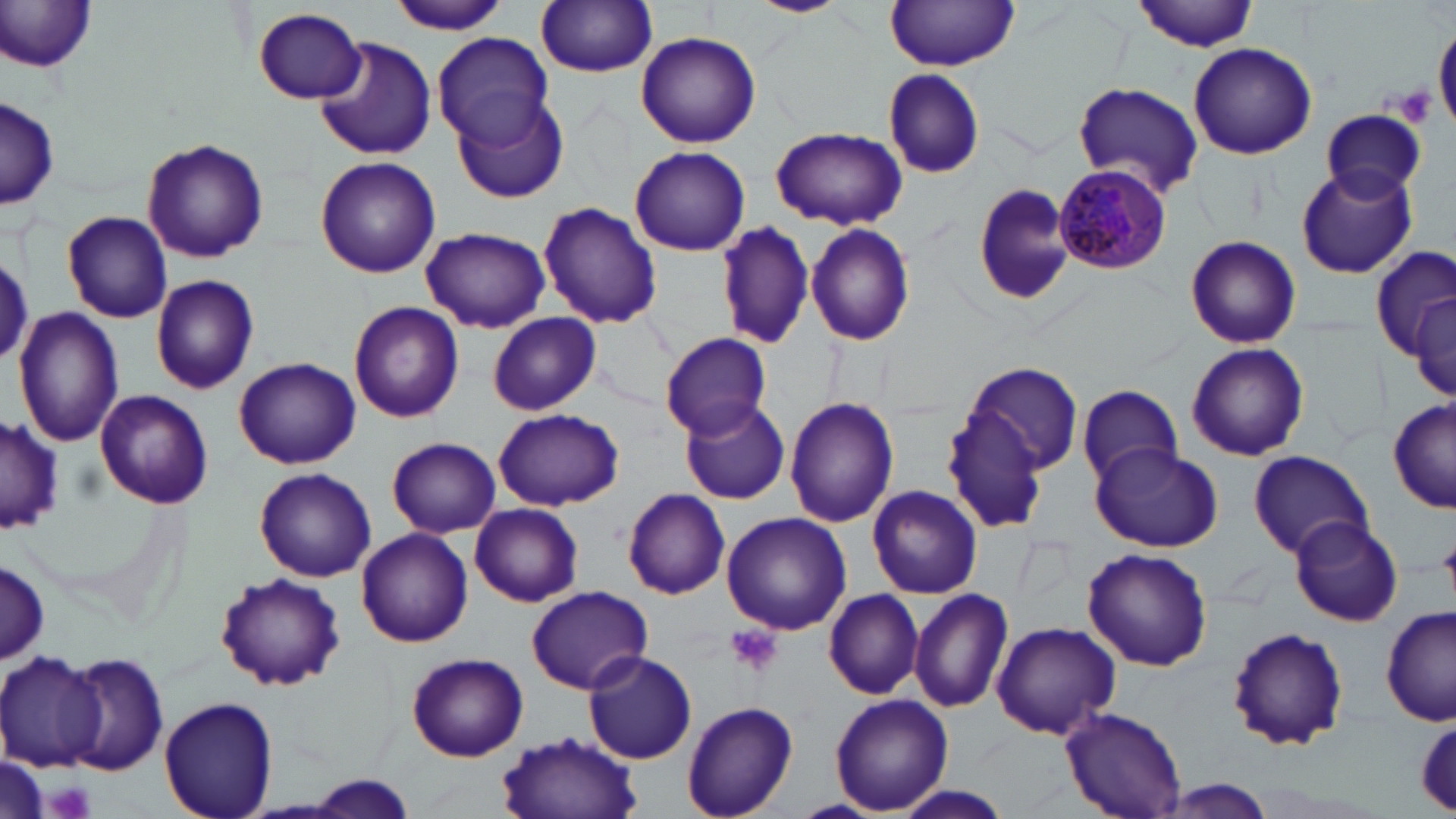
slide-level diagnosis = Plasmodium malariae
field of view = single
preparation = thin blood film
magnification = 1000x
platelet locations = approximate bounding boxes as (x1, y1, x2, y2) in pixels: (1389, 85, 1438, 128), (727, 626, 784, 677), (48, 784, 91, 817)
modality = light microscopy
Plasmodium malariae-infected red blood cell locations = approximate bounding boxes as (x1, y1, x2, y2) in pixels: (1054, 162, 1172, 275)
image size = 1456×819 pixels
stain = May-Grünwald-Giemsa
uninfected red blood cell locations = approximate bounding boxes as (x1, y1, x2, y2) in pixels: (388, 0, 510, 35), (752, 0, 845, 17), (1135, 0, 1258, 52), (536, 1, 659, 76), (0, 2, 101, 76), (886, 2, 1019, 70), (253, 8, 368, 104), (1434, 18, 1456, 136), (634, 31, 762, 149), (430, 32, 555, 147), (315, 37, 437, 160), (1187, 43, 1318, 160), (883, 69, 986, 181), (1072, 81, 1203, 198), (1, 95, 58, 213), (452, 95, 573, 205), (1319, 111, 1425, 201), (772, 126, 906, 230), (141, 137, 269, 264), (629, 144, 750, 255), (315, 157, 439, 278), (1296, 165, 1417, 278), (974, 180, 1077, 307), (538, 202, 662, 328), (63, 210, 172, 323), (717, 221, 816, 351), (805, 223, 916, 347), (420, 226, 550, 333), (1185, 234, 1302, 349), (1372, 245, 1455, 360), (0, 250, 33, 371), (151, 274, 260, 396), (1407, 288, 1456, 408), (348, 302, 465, 424), (13, 308, 125, 448), (488, 311, 600, 417), (661, 332, 773, 439), (1186, 342, 1310, 462), (234, 358, 361, 469), (961, 361, 1085, 476), (1078, 384, 1181, 485), (95, 390, 212, 509), (785, 395, 898, 528), (680, 396, 792, 505), (1388, 399, 1456, 513), (942, 407, 1054, 537), (492, 408, 623, 511), (0, 413, 63, 534), (386, 438, 501, 539), (1090, 442, 1224, 550), (1249, 449, 1372, 559), (255, 467, 377, 582), (867, 485, 983, 599), (623, 488, 731, 599), (470, 503, 583, 607), (721, 512, 851, 635), (1289, 516, 1403, 627), (355, 528, 473, 648), (1083, 547, 1212, 672), (1, 560, 49, 663), (215, 574, 345, 690), (525, 585, 654, 694), (910, 588, 1012, 713), (824, 589, 924, 699), (1382, 607, 1456, 726), (990, 621, 1120, 739), (1225, 625, 1350, 753), (584, 649, 698, 764), (0, 650, 108, 769), (405, 651, 529, 762), (63, 652, 170, 775), (829, 694, 954, 814), (159, 696, 279, 819), (680, 701, 798, 819), (1061, 707, 1185, 819), (1412, 715, 1456, 811), (497, 731, 644, 819), (295, 774, 424, 816), (1157, 778, 1280, 818), (888, 781, 1017, 819)